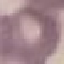
{
  "result": "no malaria parasites seen",
  "preparation": "thin blood film",
  "stain": "Giemsa",
  "image_type": "cell patch, automatically extracted from a larger field of view and resized to 64 × 64 pixels",
  "capture": "smartphone camera at the microscope eyepiece"
}